Assess for malaria.
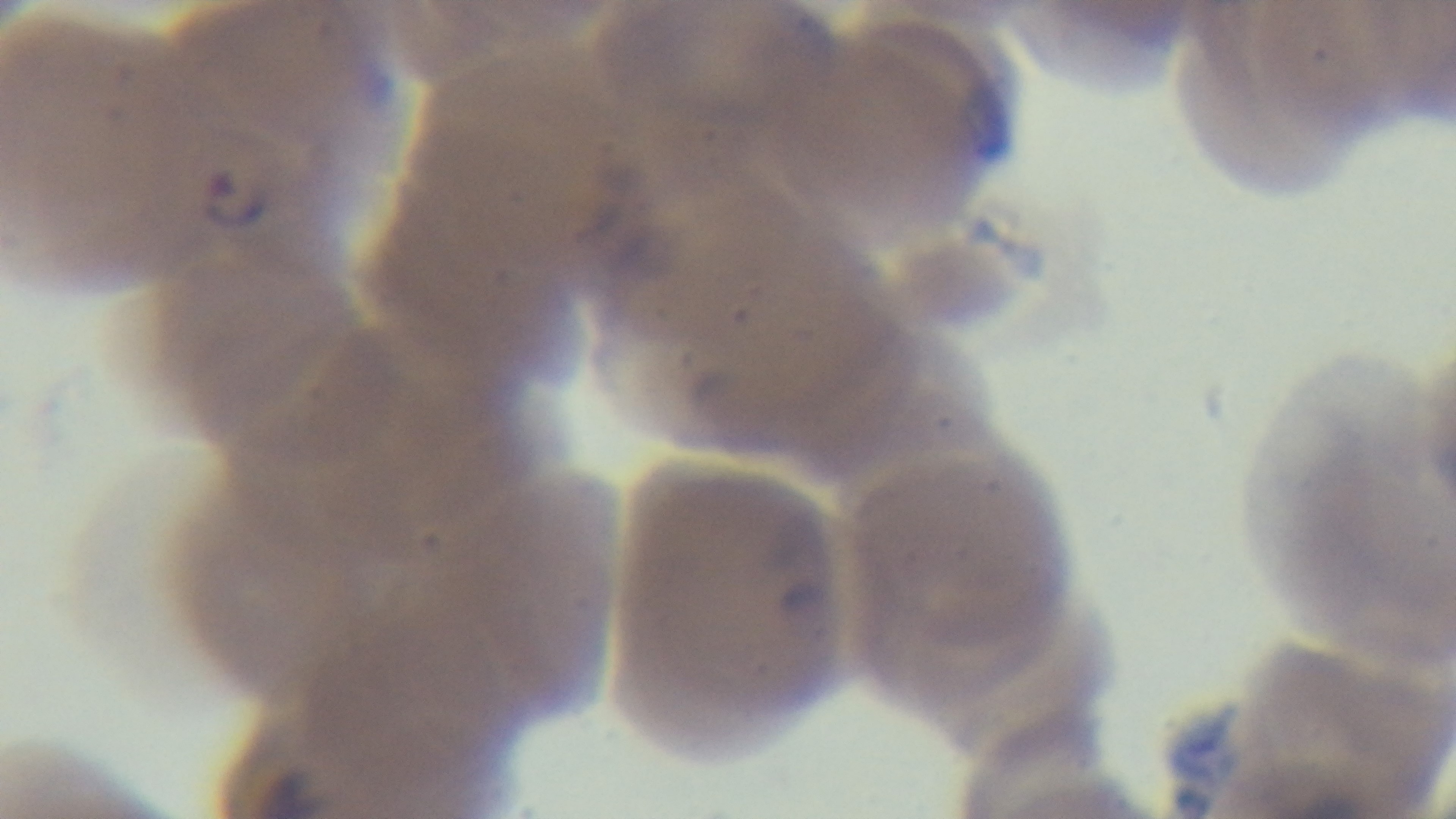

Positive.

field_of_view: one from the slide
objective: 100x oil immersion
stain: Giemsa
capture: mounted 4K digital camera
modality: light microscopy
preparation: thin